Describe the morphology of the red blood cells.
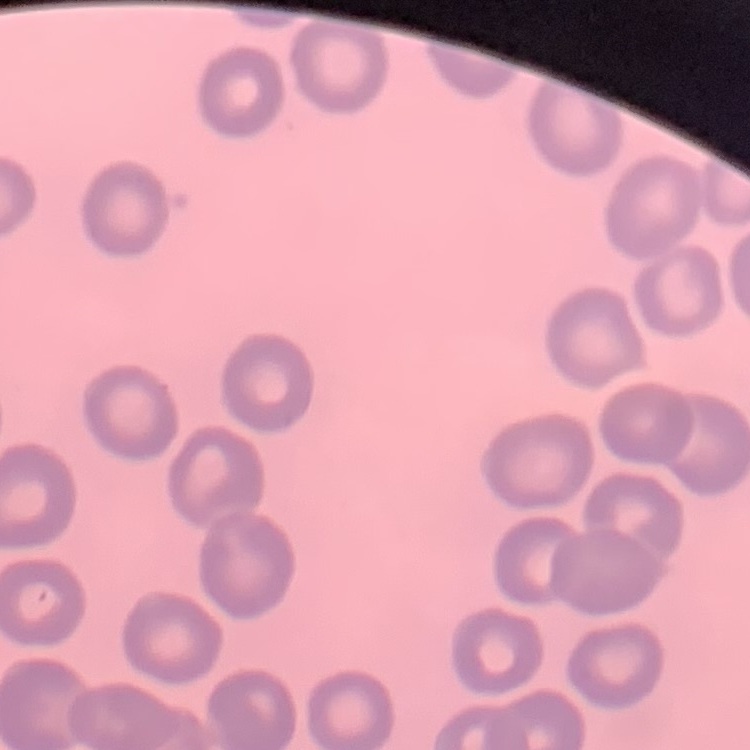

They show no rouleaux formation.

Thin peripheral smear. Square crop of a larger photomicrograph. Stained with either Field's or Giemsa.